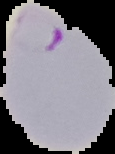

{
  "image_type": "cell region segmented out of the field of view; surrounding area masked to black",
  "preparation": "thin blood smear",
  "image_size": "115×154 pixels",
  "result": "Plasmodium parasites identified"
}